Locate every malaria parasite and every leukocyte.
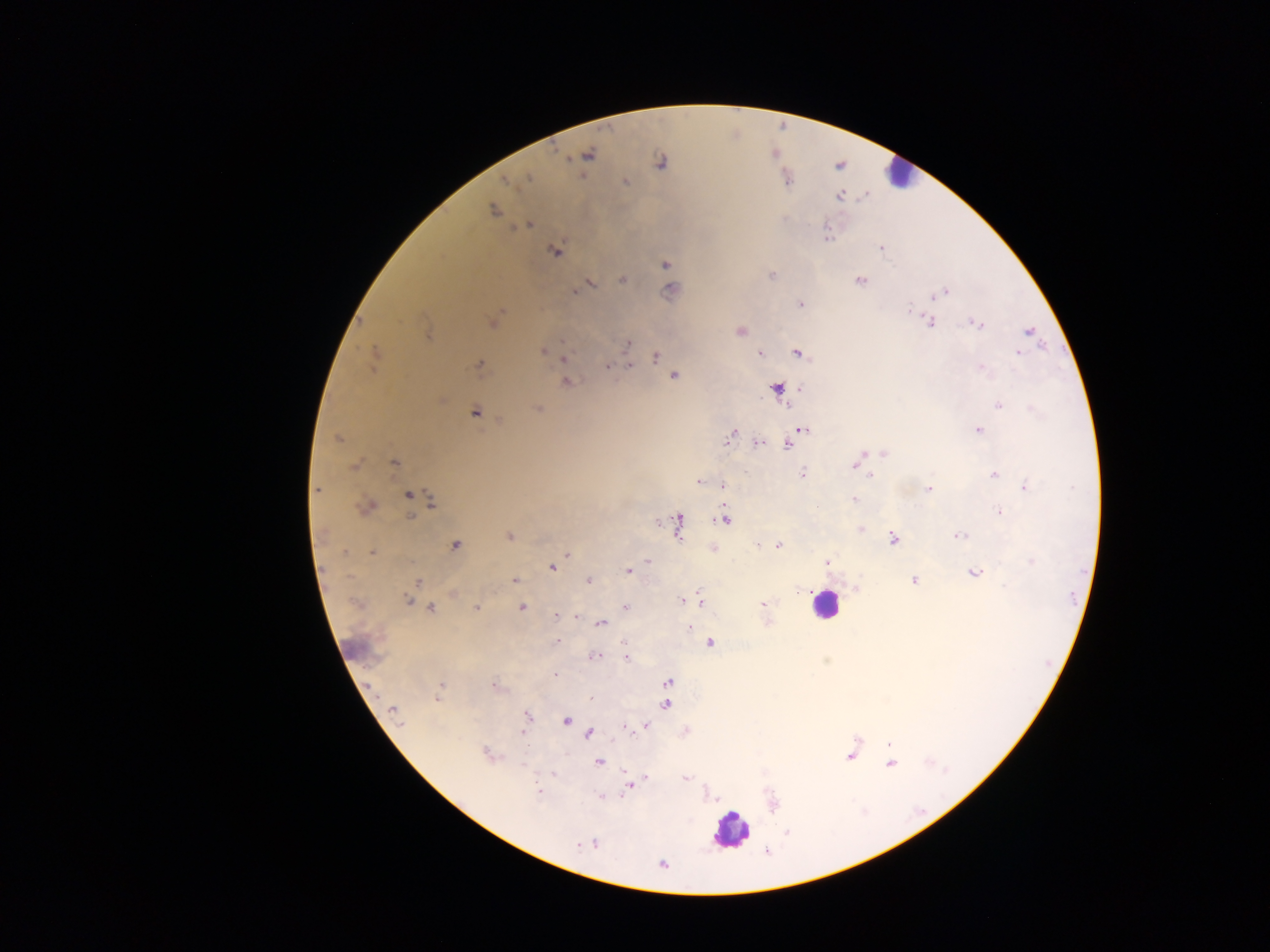
Approximate centers as x y in pixels.
Malaria parasites: 588 155; 660 163; 529 177; 505 182; 625 182; 788 182; 839 195; 493 210; 529 225; 826 237; 881 247; 555 252; 665 264; 772 276; 621 279; 860 280; 591 285; 670 291; 574 292; 947 292; 936 295; 800 304; 908 309; 930 322; 493 323; 977 323; 740 331; 1027 331; 428 336; 627 342; 543 350; 1019 350; 374 353; 799 353; 761 354; 1018 354; 656 357; 564 359; 479 365; 629 365; 607 366; 980 367; 674 376; 567 382; 778 389; 998 405; 538 409; 474 413; 803 430; 979 430; 730 436; 337 438; 759 443; 788 444; 883 453; 862 454; 394 463; 853 464; 353 467; 803 474; 994 475; 870 476; 699 482; 723 485; 1025 488; 317 490; 929 490; 408 495; 854 499; 431 501; 367 507; 999 512; 410 517; 724 518; 678 522; 658 523; 861 530; 509 536; 959 536; 893 539; 455 545; 758 545; 778 545; 345 553; 371 553; 567 555; 648 561; 1031 561; 827 563; 552 567; 628 571; 974 573; 589 580; 418 581; 515 581; 914 581; 700 598; 407 601; 682 601; 763 604; 522 607; 625 607; 477 608; 431 609; 556 616; 576 617; 601 624; 688 628; 557 641; 710 643; 594 656; 626 657; 555 674; 668 682; 441 686; 494 686; 437 698; 591 698; 665 704; 393 710; 527 715; 565 721; 646 725; 627 729; 523 732; 589 733; 889 744; 486 754; 850 756; 599 762; 891 764; 554 774; 646 777; 686 778; 630 787; 538 791; 599 798; 578 844; 595 844; 662 864.
Leukocytes: 898 173; 824 605; 355 649; 730 831.

Summary:
  - Preparation: thick blood film
  - Image size: 1270×952 pixels
  - Country: Ghana
  - Field of view: single
  - Capture: mobile-phone photograph through a microscope